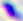

Summary:
  - Modality: micrograph
  - Magnification: 400x
  - Identification: Toxoplasma gondii